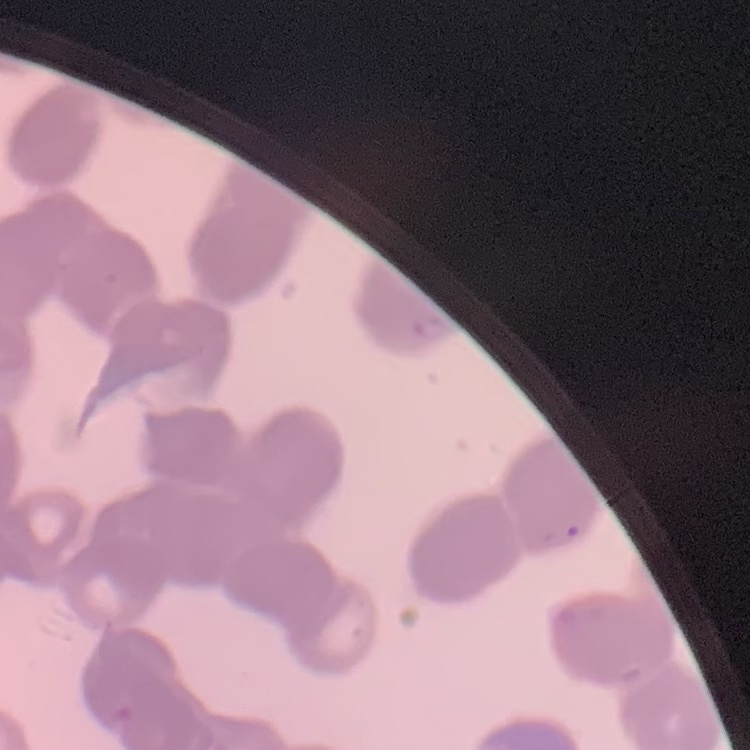
The red blood cells exhibit rouleaux formation. Stained with either Field's or Giemsa. Thin blood film. Square crop of a larger photomicrograph.